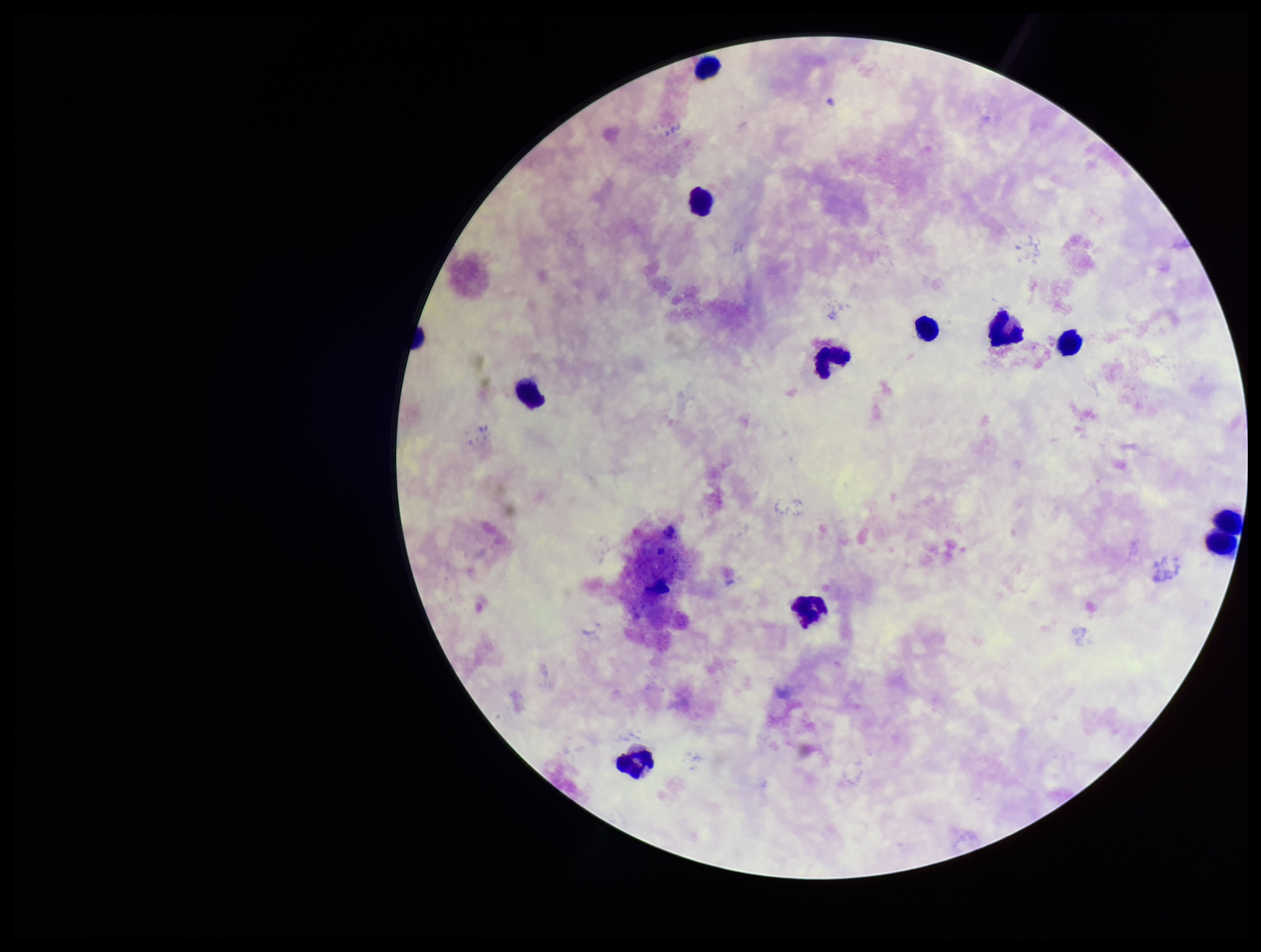 Patient malaria status: negative. Leukocyte count: 10. Single field of view. Stained with Giemsa. Plasmodium parasites: none detected. Image is 1261×952 pixels. Preparation: thick blood smear. Parasite count: 0. Photographed through the microscope eyepiece with a smartphone camera.